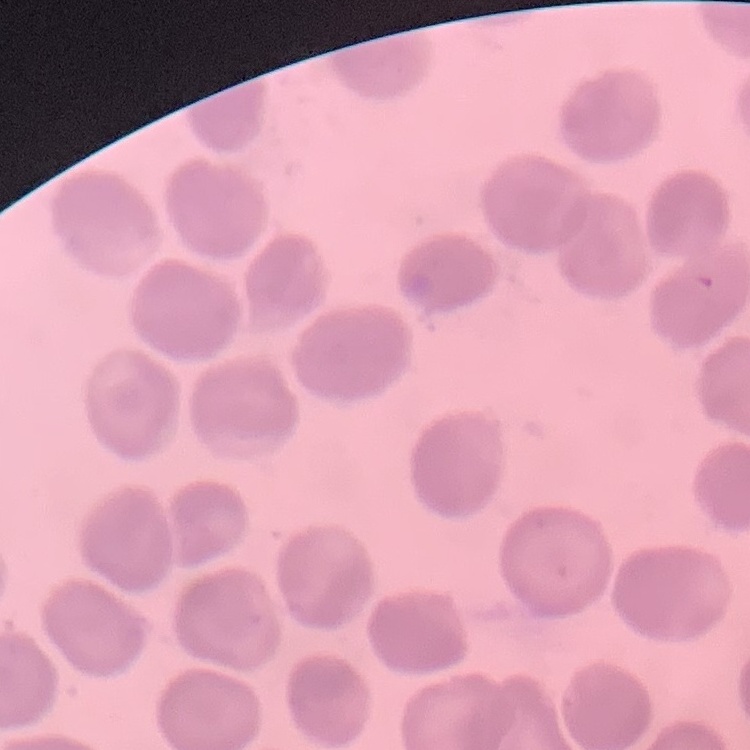
The red blood cells exhibit no rouleaux formation. One tile cut from a larger photomicrograph. Stained with either Field's or Giemsa. Thin peripheral smear.